Outline each blood parasite and name the species.
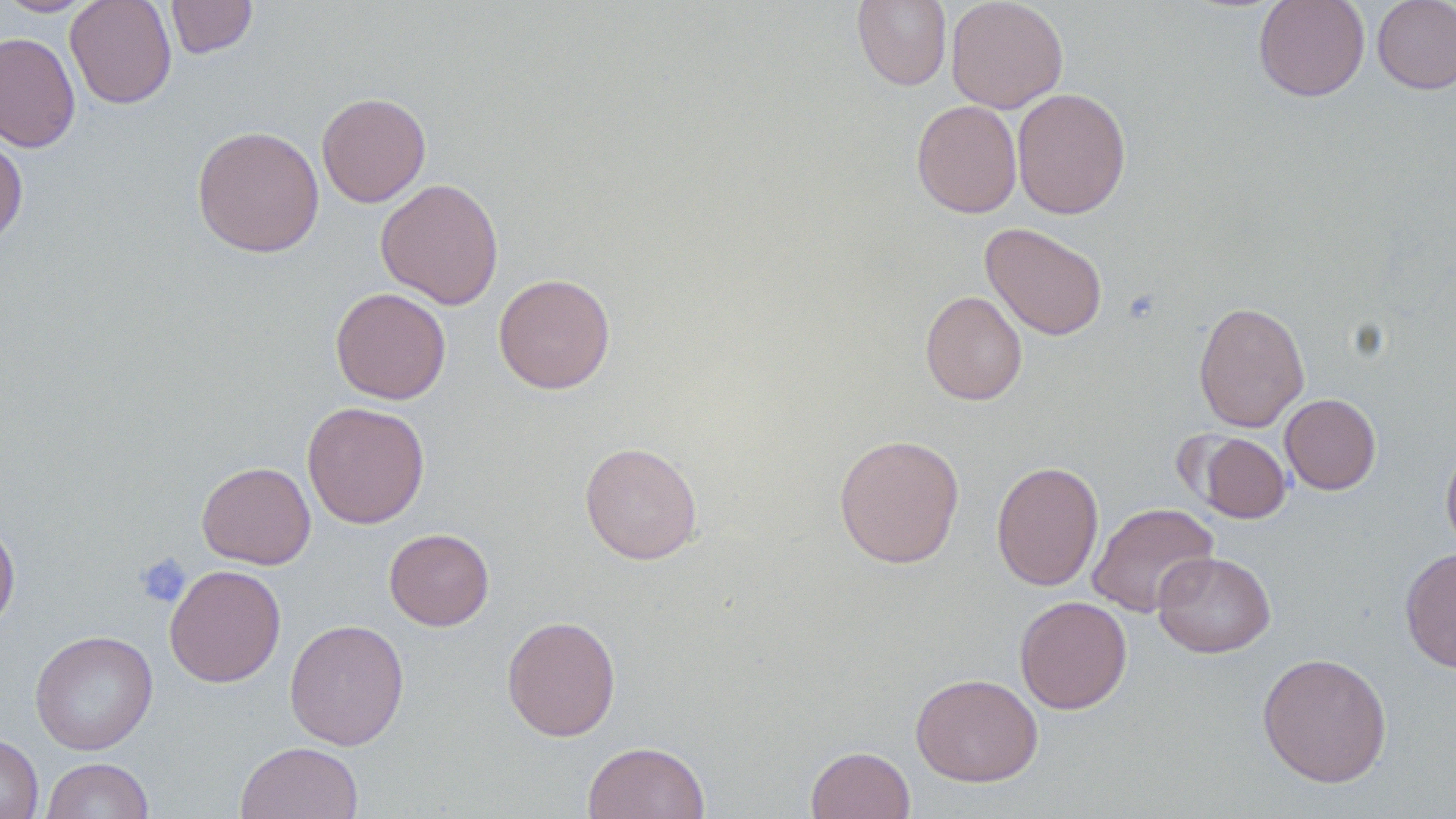

No blood parasites observed.

Summary:
  - Coordinate format: approximate bounding boxes as named x1/y1/x2/y2 corners in pixels
  - Uninfected red blood cell locations: (x1=0, y1=0, x2=99, y2=17), (x1=64, y1=0, x2=177, y2=109), (x1=165, y1=0, x2=258, y2=59), (x1=851, y1=0, x2=952, y2=91), (x1=946, y1=0, x2=1068, y2=113), (x1=1253, y1=0, x2=1370, y2=102), (x1=1372, y1=0, x2=1456, y2=94), (x1=0, y1=31, x2=81, y2=153), (x1=1011, y1=87, x2=1131, y2=220), (x1=316, y1=92, x2=431, y2=207), (x1=911, y1=100, x2=1022, y2=218), (x1=191, y1=125, x2=324, y2=257), (x1=0, y1=135, x2=28, y2=249), (x1=375, y1=178, x2=504, y2=309), (x1=981, y1=222, x2=1108, y2=340), (x1=494, y1=273, x2=616, y2=394), (x1=330, y1=287, x2=451, y2=405), (x1=920, y1=290, x2=1028, y2=405), (x1=1193, y1=300, x2=1309, y2=433), (x1=1280, y1=393, x2=1381, y2=494), (x1=302, y1=401, x2=430, y2=529), (x1=1192, y1=431, x2=1291, y2=524), (x1=833, y1=433, x2=965, y2=569), (x1=1440, y1=439, x2=1456, y2=558), (x1=579, y1=441, x2=703, y2=564), (x1=990, y1=460, x2=1104, y2=591), (x1=197, y1=461, x2=316, y2=569), (x1=1088, y1=502, x2=1218, y2=617), (x1=0, y1=517, x2=20, y2=633), (x1=384, y1=528, x2=494, y2=630), (x1=1400, y1=547, x2=1456, y2=674), (x1=1152, y1=551, x2=1276, y2=658), (x1=165, y1=564, x2=286, y2=688), (x1=1014, y1=595, x2=1132, y2=714), (x1=502, y1=615, x2=621, y2=742), (x1=284, y1=619, x2=409, y2=750), (x1=30, y1=630, x2=158, y2=755), (x1=1257, y1=652, x2=1393, y2=788), (x1=910, y1=673, x2=1043, y2=787), (x1=0, y1=733, x2=43, y2=819), (x1=235, y1=741, x2=363, y2=819), (x1=583, y1=741, x2=710, y2=819), (x1=806, y1=745, x2=915, y2=819), (x1=41, y1=757, x2=155, y2=818)
  - Platelet locations: (x1=134, y1=553, x2=192, y2=608)
  - Slide-level diagnosis: no evidence of blood parasites
  - Modality: light microscopy
  - Magnification: 1000x
  - Preparation: thin blood film
  - Field of view: one of a larger specimen
  - Stain: May-Grünwald-Giemsa
  - Image size: 1456×819 pixels